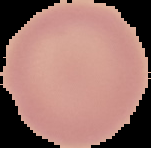
From a thin blood smear. Result: no Plasmodium parasites detected. Image is 151×148 pixels. Segmented cell region on a black background.